Point out each Plasmodium parasite.
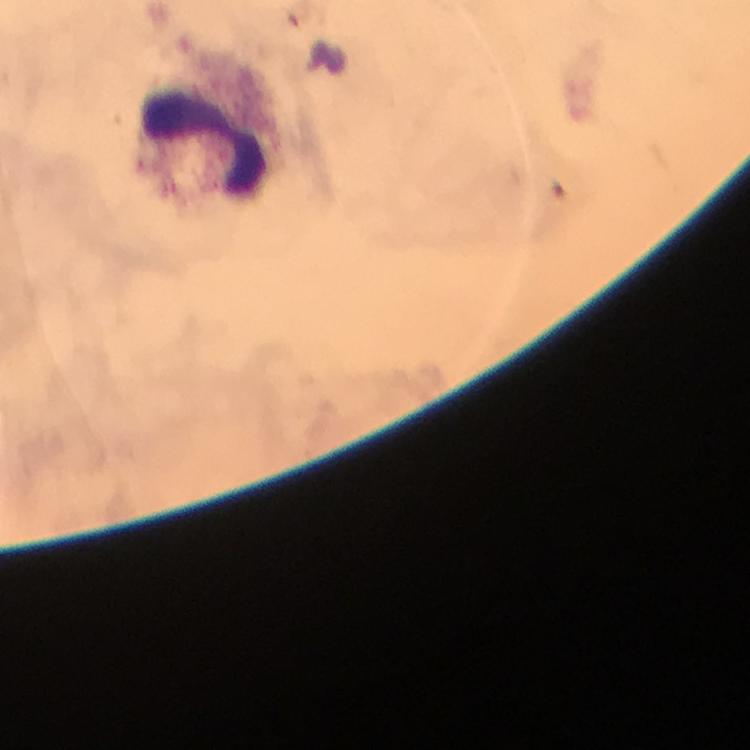

No Plasmodium parasites seen.

Approximate centers as [x, y] in pixels.
Summary:
  - Leukocyte locations: [206, 143]
  - Preparation: thick blood film
  - Magnification: 100x
  - Immersion oil: applied
  - Capture: smartphone mounted on the microscope
  - Image size: 750×750 pixels
  - Context: from a diagnostic examination for malaria
  - Cropped from: a single field of view
  - Stain: Giemsa